Report the malaria status of this cell.
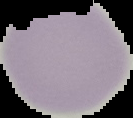

It is uninfected.

Summary:
  - Image type: cell region segmented out of the field of view; surrounding area masked to black
  - Preparation: thin blood smear
  - Image size: 133×118 pixels